Report the malaria status of this cell.
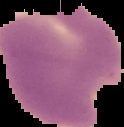

Parasitized.

image type = segmented cell region on a black background
image size = 124×127 pixels
preparation = thin blood smear